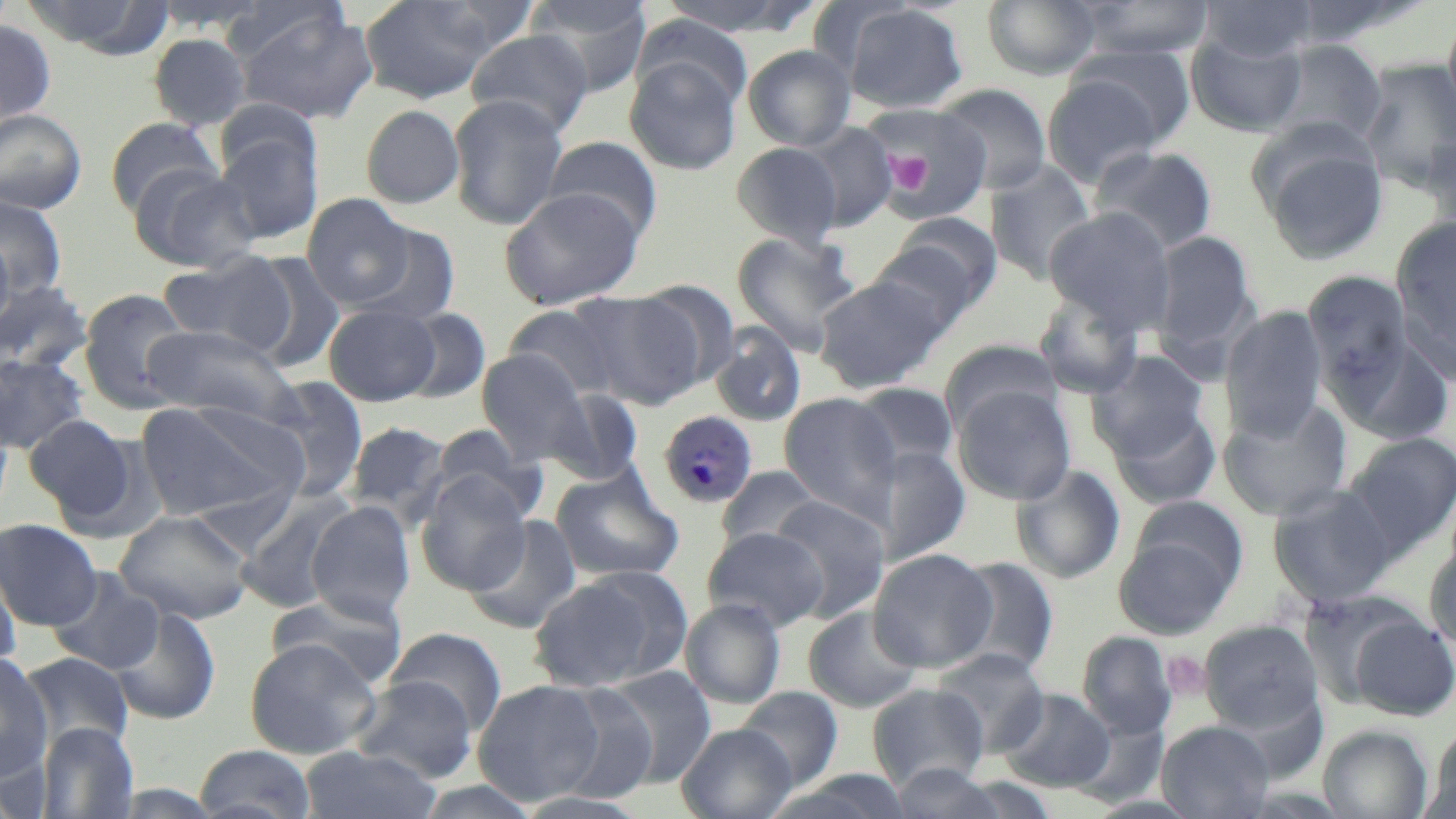

slide-level diagnosis = Plasmodium malariae
image size = 1456×819 pixels
Plasmodium malariae-infected red blood cell locations = approximate bounding boxes as (x1,y1)-(x2,y2) corner pairs in pixels: (658,411)-(757,508)
magnification = 1000x
stain = May-Grünwald-Giemsa
platelet locations = approximate bounding boxes as (x1,y1)-(x2,y2) corner pairs in pixels: (882,150)-(935,194), (1162,651)-(1210,699)
field of view = single
modality = optical microscopy
uninfected red blood cell locations = approximate bounding boxes as (x1,y1)-(x2,y2) corner pairs in pixels: (19,0)-(174,57), (359,0)-(499,104), (525,0)-(653,97), (655,0)-(815,36), (981,0)-(1100,80), (1074,0)-(1215,60), (1199,0)-(1320,62), (1284,0)-(1429,48), (840,4)-(968,113), (232,6)-(378,125), (1443,12)-(1456,122), (632,16)-(752,111), (0,17)-(58,132), (465,29)-(594,138), (1186,31)-(1307,136), (147,33)-(251,131), (1268,39)-(1389,146), (743,44)-(856,151), (1070,44)-(1196,148), (624,57)-(742,176), (1359,58)-(1456,191), (1042,76)-(1164,188), (936,84)-(1052,194), (447,93)-(569,231), (865,104)-(992,221), (360,105)-(465,209), (0,108)-(87,214), (214,115)-(325,247), (105,117)-(224,217), (800,122)-(898,232), (1421,131)-(1456,235), (542,136)-(662,241), (731,141)-(843,249), (1259,141)-(1389,266), (1089,145)-(1218,254), (985,161)-(1097,284), (131,164)-(261,273), (499,187)-(645,309), (301,193)-(415,309), (1,195)-(68,301), (1043,207)-(1176,332), (1392,216)-(1456,343), (870,223)-(998,333), (355,224)-(461,326), (731,231)-(861,357), (1150,231)-(1258,354), (0,233)-(16,341), (843,245)-(982,373), (157,251)-(296,356), (244,251)-(346,372), (1303,271)-(1414,402), (814,273)-(948,393), (0,279)-(93,376), (78,288)-(194,413), (1034,290)-(1145,400), (573,291)-(704,411), (324,304)-(440,406), (504,304)-(620,402), (1220,305)-(1328,441), (398,307)-(491,404), (141,322)-(300,427), (709,324)-(807,427), (1338,335)-(1456,447), (938,340)-(1063,435), (477,349)-(594,465), (1089,351)-(1211,461), (0,352)-(92,455), (262,377)-(369,501), (849,382)-(960,479), (953,385)-(1076,505), (543,389)-(646,484), (778,393)-(903,524), (1218,397)-(1353,522), (135,399)-(305,524), (1110,404)-(1222,511), (22,414)-(138,522), (345,421)-(451,525), (434,425)-(544,524), (1343,432)-(1456,556), (880,446)-(971,566), (1011,464)-(1126,584), (716,466)-(827,554), (551,469)-(685,582), (416,472)-(532,594), (1267,483)-(1397,606), (236,489)-(358,613), (769,495)-(890,621), (306,502)-(415,622), (114,510)-(254,625), (465,514)-(583,635), (0,518)-(103,630), (1114,523)-(1239,638), (703,526)-(829,631), (1424,544)-(1456,654), (868,548)-(996,672), (0,556)-(22,676), (950,556)-(1059,676), (46,568)-(166,676), (527,569)-(682,692), (267,591)-(408,690), (680,598)-(786,709), (108,605)-(222,726), (803,606)-(924,712), (1349,613)-(1456,721), (1200,620)-(1323,732), (385,627)-(507,736), (1078,631)-(1176,738), (244,638)-(380,759), (931,648)-(1049,756), (20,651)-(134,753), (0,654)-(54,778), (604,665)-(717,788), (350,676)-(480,783), (472,679)-(606,805), (550,683)-(660,804), (867,684)-(988,790), (735,687)-(844,789), (999,689)-(1115,792), (1157,721)-(1274,818), (36,722)-(138,817), (677,723)-(796,819), (1318,725)-(1433,818), (1425,730)-(1456,819), (193,744)-(317,819), (298,745)-(440,819), (0,747)-(48,819), (886,763)-(1011,818), (776,770)-(916,819), (413,781)-(544,819), (511,791)-(654,819)
preparation = thin blood smear